Report the malaria status of this cell.
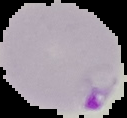
It is parasitized.

image size = 127×118 pixels
preparation = thin blood smear
image type = segmented cell region on a black background